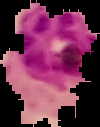
Summary:
  - Malaria status: parasitized
  - Image size: 100×127 pixels
  - Image type: segmented cell region on a black background
  - Preparation: thin blood film